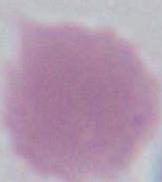

Captured at 1000x magnification. Micrograph. A red blood cell is shown.